Classify this cell by malaria status.
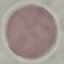
It is uninfected.

Cell patch, automatically extracted from a larger field of view and resized to 64 × 64 pixels. Thin blood film. Giemsa-stained preparation. Acquired by smartphone through the microscope eyepiece.